Locate every Plasmodium parasite.
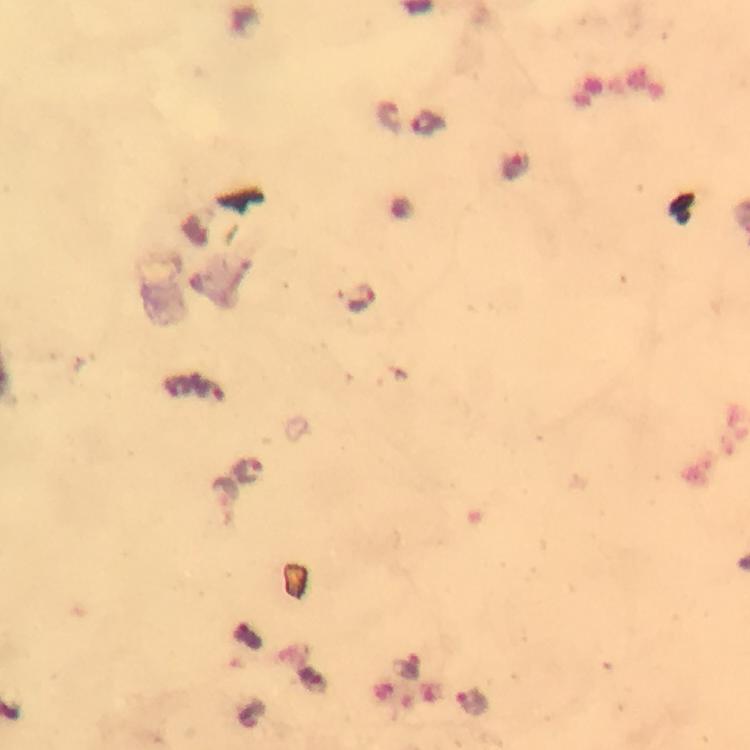
Approximate object centers, in pixels from the top-left corner.
Plasmodium parasites: (x=359, y=298), (x=250, y=469), (x=471, y=703).

From a diagnostic examination for malaria. Giemsa-stained preparation. Image is 750×750 pixels. Smartphone photograph taken through a microscope. 100x magnification. A crop from one field of view. Immersion oil applied. Thick blood film.